State which parasite is depicted.
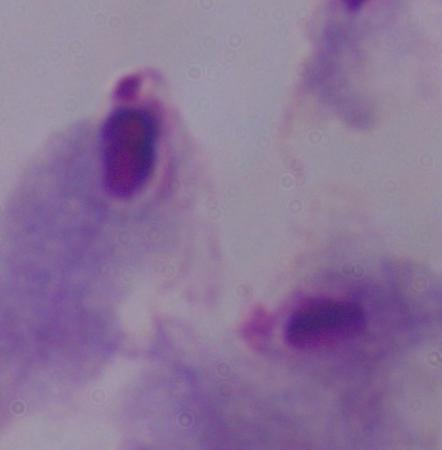

This is a trichomonad.

Micrograph. Captured at 1000x magnification.